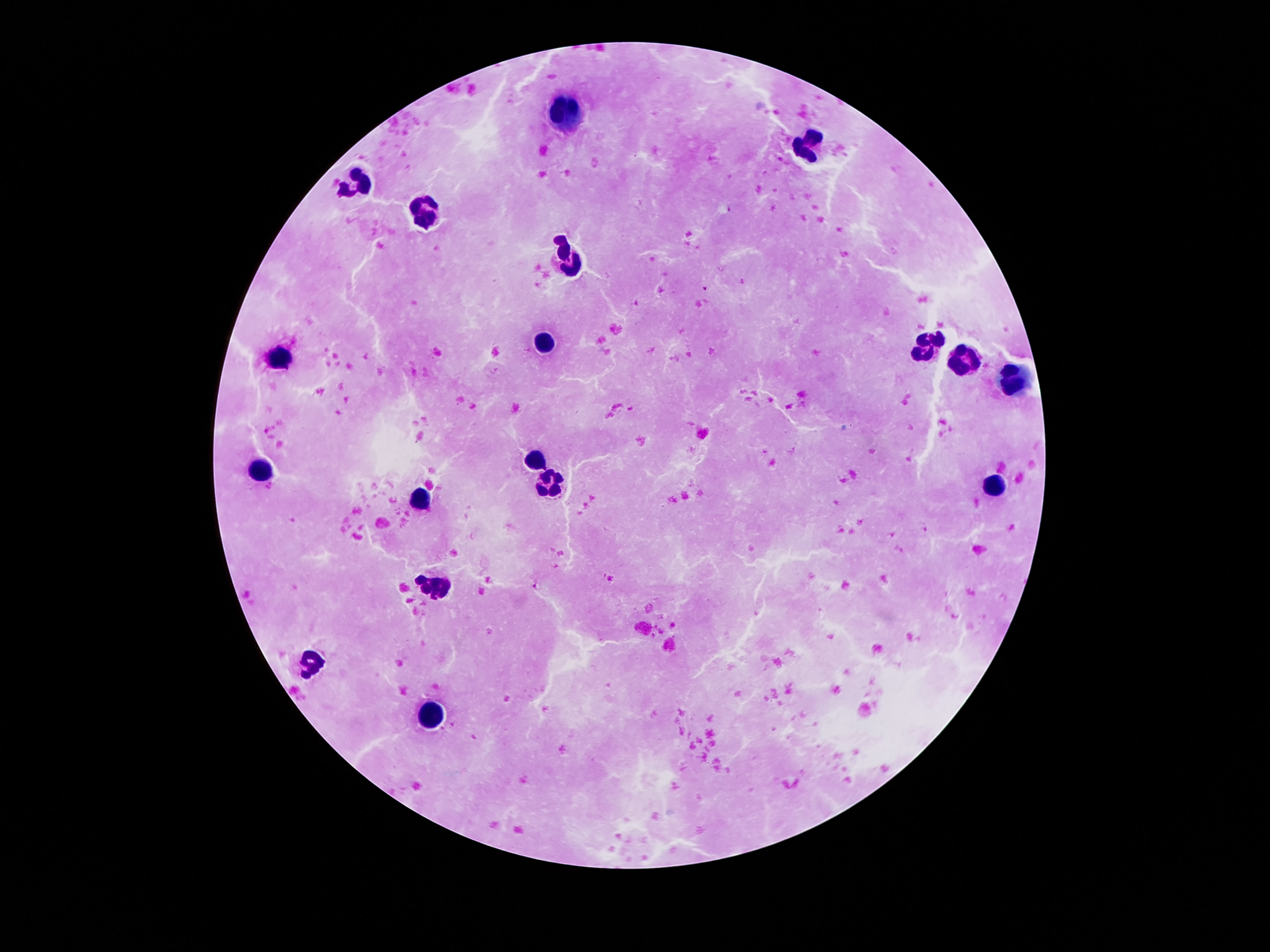 Approximate object centers, in pixels from the top-left corner. Leukocyte locations: (x=567, y=114), (x=808, y=146), (x=359, y=181), (x=427, y=213), (x=570, y=252), (x=545, y=339), (x=926, y=348), (x=284, y=356), (x=960, y=360), (x=1012, y=380), (x=536, y=462), (x=257, y=467), (x=545, y=484), (x=997, y=487), (x=420, y=499), (x=436, y=586), (x=311, y=660), (x=429, y=715). Thick peripheral-blood smear. Single field of view. 100x magnification. Giemsa-stained preparation. Image is 1270×952 pixels. Patient malaria status: uninfected. Smartphone photograph taken through the microscope eyepiece.